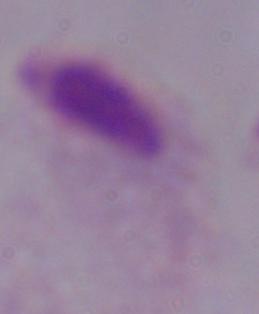

magnification = 1000x
identification = trichomonad
modality = micrograph